Classify this cell by malaria status.
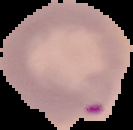

Parasitized.

Segmented cell region on a black background. Image is 133×130 pixels. From a thin blood smear.